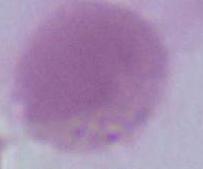

modality = photomicrograph
identification = red blood cell
magnification = 1000x